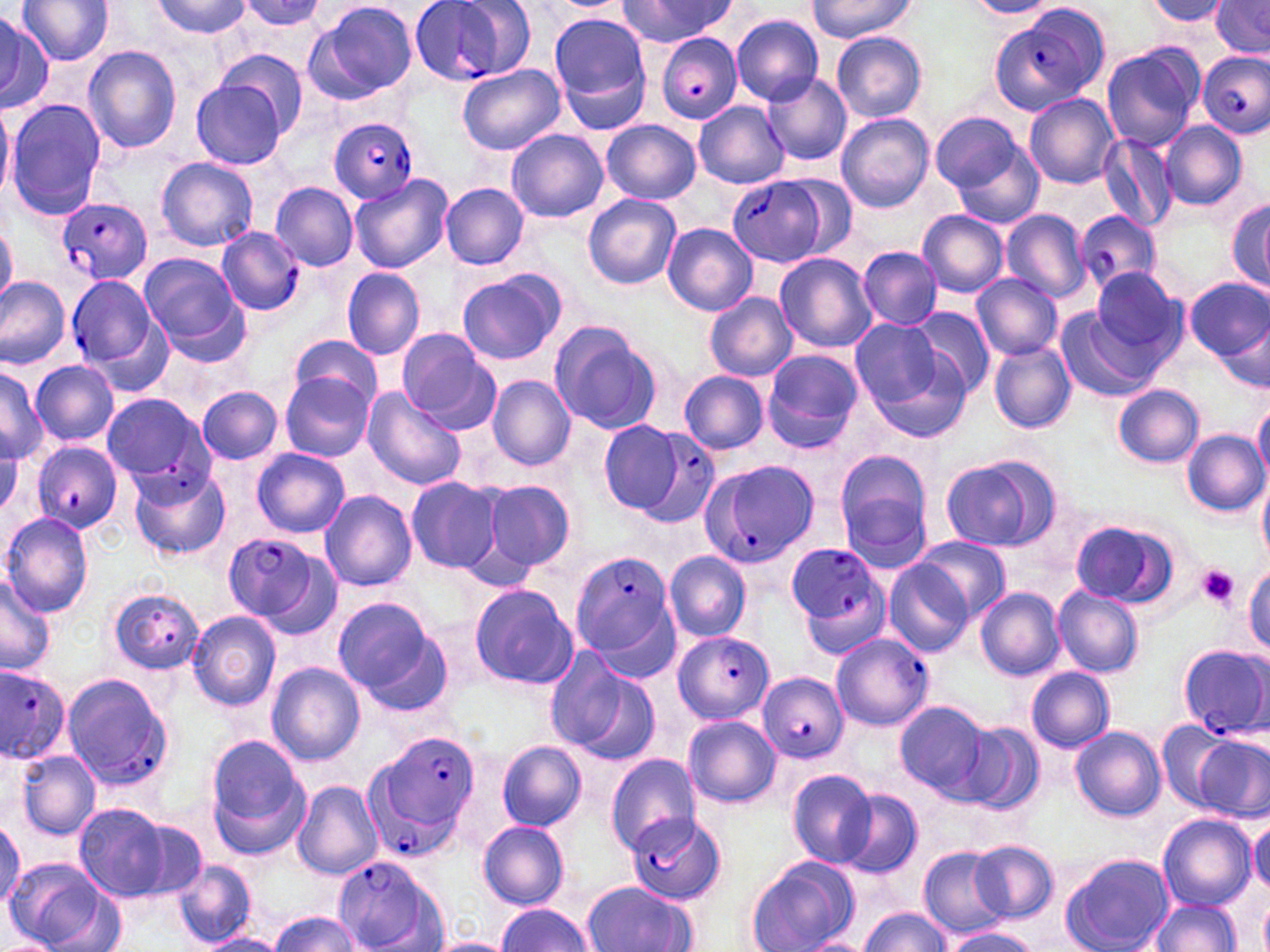
slide-level diagnosis = Plasmodium falciparum
magnification = 1000x
preparation = thin blood smear
platelet locations = approximate bounding boxes as (x1, y1, x2, y2) in pixels: (1196, 565, 1240, 611)
stain = May-Grünwald-Giemsa
image size = 1270×952 pixels
Plasmodium falciparum-infected red blood cell locations = approximate bounding boxes as (x1, y1, x2, y2) in pixels: (409, 1, 536, 86), (991, 8, 1110, 116), (656, 33, 742, 123), (1198, 50, 1270, 139), (328, 120, 419, 203), (726, 173, 839, 269), (58, 197, 151, 288), (1074, 211, 1162, 292), (217, 226, 304, 316), (66, 277, 159, 371), (130, 412, 223, 516), (628, 431, 722, 530), (30, 441, 123, 534), (697, 458, 823, 569), (223, 531, 328, 630), (785, 546, 891, 656), (570, 551, 676, 663), (106, 586, 207, 673), (827, 630, 933, 728), (674, 631, 773, 725), (1178, 644, 1269, 738), (0, 667, 71, 763), (760, 670, 847, 761), (57, 671, 172, 792), (372, 731, 481, 857), (627, 816, 727, 902), (330, 857, 450, 952)
field of view = one of a larger specimen
modality = light microscopy
uninfected red blood cell locations = approximate bounding boxes as (x1, y1, x2, y2) in pixels: (18, 0, 114, 66), (153, 0, 251, 39), (236, 0, 326, 33), (307, 0, 418, 103), (619, 0, 736, 47), (807, 0, 919, 41), (1209, 0, 1269, 57), (964, 1, 1062, 19), (1141, 1, 1234, 30), (549, 13, 650, 113), (0, 14, 51, 112), (731, 16, 825, 104), (831, 31, 927, 122), (1100, 41, 1204, 151), (83, 46, 181, 154), (217, 49, 308, 137), (458, 63, 565, 155), (761, 72, 852, 165), (190, 73, 294, 169), (1024, 93, 1120, 188), (5, 100, 105, 219), (694, 102, 789, 189), (0, 103, 13, 201), (929, 111, 1026, 196), (835, 113, 935, 213), (602, 120, 701, 204), (1159, 121, 1248, 211), (507, 129, 608, 222), (945, 131, 1045, 228), (1098, 135, 1178, 231), (157, 158, 258, 252), (349, 174, 452, 274), (271, 183, 357, 270), (440, 183, 529, 270), (584, 194, 681, 290), (1225, 194, 1270, 297), (916, 209, 1008, 298), (1000, 209, 1091, 302), (0, 220, 18, 309), (662, 223, 758, 315), (857, 246, 942, 329), (139, 252, 251, 361), (774, 252, 878, 354), (342, 267, 426, 360), (1091, 267, 1186, 362), (457, 268, 568, 366), (973, 272, 1062, 361), (0, 277, 70, 372), (1184, 278, 1269, 363), (705, 293, 796, 381), (903, 308, 995, 401), (1055, 308, 1150, 402), (850, 319, 944, 408), (546, 321, 662, 436), (395, 328, 498, 431), (290, 335, 382, 410), (858, 336, 974, 442), (988, 342, 1077, 434), (761, 349, 864, 453), (30, 359, 118, 447), (0, 367, 44, 462), (678, 370, 770, 455), (279, 372, 373, 461), (488, 376, 575, 470), (1113, 384, 1204, 468), (198, 387, 281, 463), (361, 387, 465, 490), (101, 393, 209, 486), (1253, 399, 1270, 485), (599, 420, 687, 515), (1183, 430, 1268, 516), (253, 448, 350, 537), (834, 449, 933, 561), (939, 454, 1058, 551), (129, 466, 231, 563), (1257, 474, 1270, 563), (407, 476, 502, 574), (480, 478, 575, 574), (320, 490, 417, 592), (1, 513, 95, 617), (1068, 520, 1167, 606), (913, 536, 1012, 625), (664, 551, 751, 641), (883, 559, 974, 657), (1245, 563, 1270, 653), (0, 570, 56, 675), (468, 583, 576, 688), (976, 586, 1066, 680), (1051, 586, 1144, 678), (332, 597, 440, 697), (187, 609, 281, 710), (546, 651, 654, 763), (265, 662, 365, 765), (1026, 667, 1116, 752), (895, 699, 994, 799), (684, 714, 780, 806), (1156, 719, 1235, 810), (960, 722, 1045, 815), (1070, 726, 1165, 821), (204, 737, 311, 858), (1196, 738, 1268, 818), (498, 740, 586, 830), (15, 749, 101, 842), (608, 754, 701, 853), (788, 769, 878, 867), (292, 780, 383, 881), (837, 787, 923, 879), (73, 803, 177, 902), (1157, 813, 1257, 912), (1247, 818, 1270, 894), (477, 820, 570, 910), (0, 822, 24, 906), (968, 840, 1058, 922), (918, 845, 1009, 940), (1061, 853, 1174, 952), (745, 856, 860, 952), (8, 857, 108, 951), (174, 859, 257, 947), (581, 880, 700, 950), (1259, 891, 1270, 952), (1148, 897, 1241, 951), (496, 904, 596, 951), (858, 907, 951, 951), (269, 911, 363, 951), (941, 929, 1044, 952), (197, 933, 289, 952), (423, 936, 518, 952), (799, 936, 876, 952), (0, 937, 58, 952)